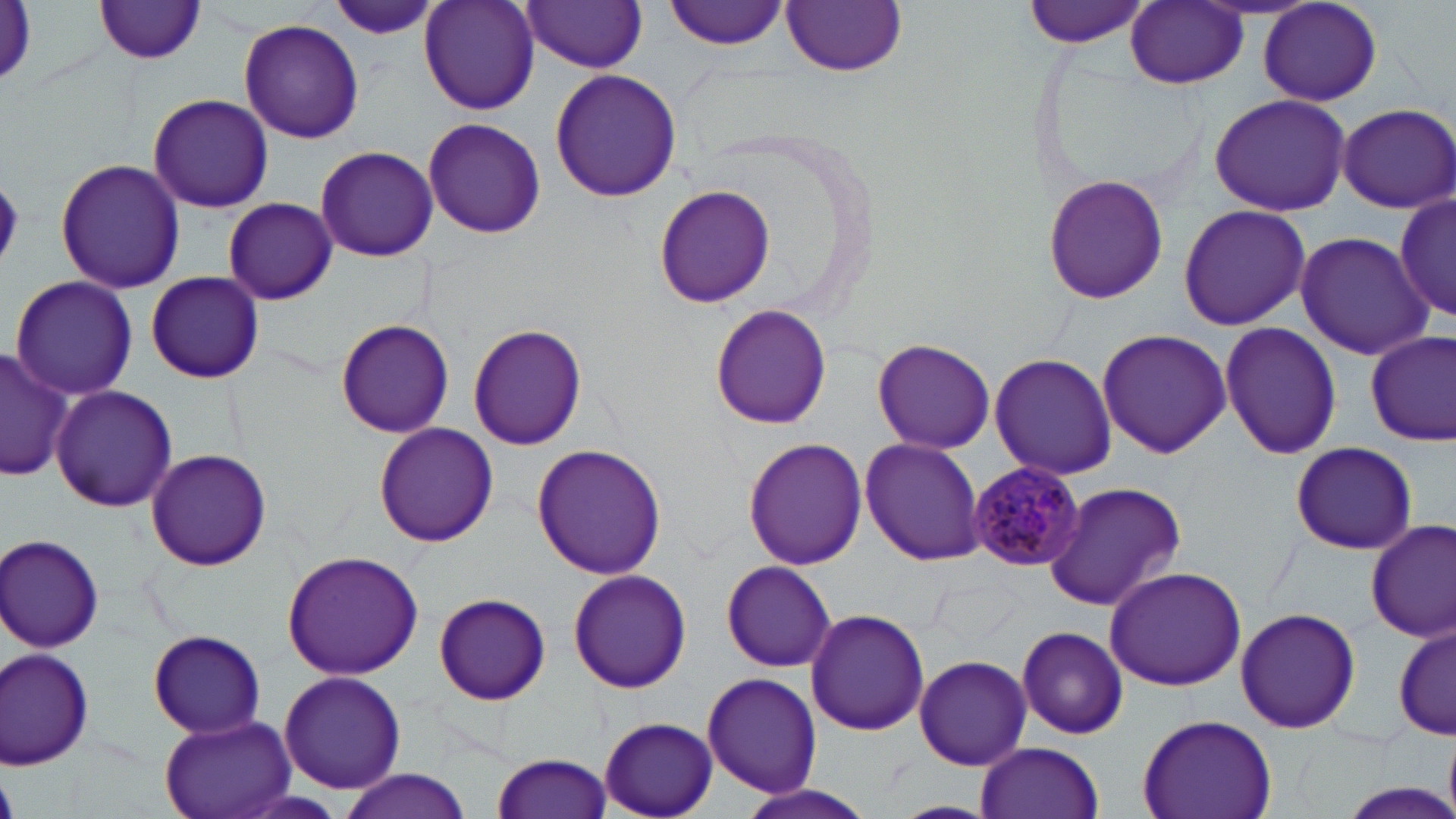

slide-level diagnosis = Plasmodium malariae
magnification = 1000x
preparation = thin blood film
modality = optical microscopy
field of view = single
stain = May-Grünwald-Giemsa
image size = 1456×819 pixels
uninfected red blood cell locations = approximate bounding boxes as named x1/y1/x2/y2 corners in pixels: (x1=419, y1=0, x2=540, y2=115), (x1=664, y1=0, x2=791, y2=50), (x1=1023, y1=0, x2=1153, y2=49), (x1=94, y1=1, x2=209, y2=64), (x1=324, y1=1, x2=442, y2=42), (x1=522, y1=1, x2=649, y2=72), (x1=782, y1=1, x2=907, y2=76), (x1=1125, y1=2, x2=1247, y2=89), (x1=1257, y1=2, x2=1383, y2=107), (x1=237, y1=20, x2=365, y2=143), (x1=550, y1=67, x2=682, y2=201), (x1=147, y1=94, x2=273, y2=212), (x1=1207, y1=94, x2=1353, y2=214), (x1=1335, y1=103, x2=1456, y2=212), (x1=422, y1=117, x2=546, y2=239), (x1=315, y1=144, x2=439, y2=261), (x1=55, y1=158, x2=186, y2=293), (x1=1044, y1=173, x2=1168, y2=304), (x1=651, y1=182, x2=775, y2=308), (x1=1392, y1=189, x2=1453, y2=325), (x1=223, y1=197, x2=337, y2=305), (x1=1177, y1=203, x2=1312, y2=331), (x1=1295, y1=231, x2=1433, y2=359), (x1=144, y1=272, x2=264, y2=383), (x1=10, y1=275, x2=139, y2=401), (x1=709, y1=304, x2=832, y2=430), (x1=335, y1=319, x2=455, y2=438), (x1=1219, y1=321, x2=1343, y2=458), (x1=468, y1=322, x2=588, y2=450), (x1=1097, y1=328, x2=1232, y2=458), (x1=1364, y1=328, x2=1455, y2=445), (x1=873, y1=338, x2=995, y2=454), (x1=0, y1=347, x2=74, y2=484), (x1=988, y1=351, x2=1119, y2=480), (x1=51, y1=385, x2=178, y2=512), (x1=375, y1=423, x2=499, y2=546), (x1=859, y1=438, x2=986, y2=566), (x1=743, y1=439, x2=868, y2=571), (x1=1286, y1=441, x2=1419, y2=554), (x1=531, y1=443, x2=667, y2=580), (x1=145, y1=447, x2=273, y2=571), (x1=1043, y1=481, x2=1187, y2=613), (x1=1366, y1=517, x2=1456, y2=644), (x1=2, y1=534, x2=105, y2=651), (x1=281, y1=550, x2=425, y2=681), (x1=718, y1=561, x2=839, y2=673), (x1=1103, y1=565, x2=1247, y2=690), (x1=567, y1=568, x2=692, y2=693), (x1=432, y1=592, x2=552, y2=706), (x1=1235, y1=606, x2=1361, y2=736), (x1=806, y1=607, x2=928, y2=736), (x1=1392, y1=617, x2=1453, y2=743), (x1=1013, y1=626, x2=1129, y2=740), (x1=148, y1=630, x2=265, y2=738), (x1=1, y1=648, x2=96, y2=771), (x1=913, y1=653, x2=1033, y2=772), (x1=278, y1=670, x2=406, y2=793), (x1=700, y1=672, x2=821, y2=797), (x1=1137, y1=712, x2=1277, y2=819), (x1=157, y1=714, x2=296, y2=819), (x1=598, y1=716, x2=718, y2=818), (x1=975, y1=741, x2=1104, y2=819), (x1=492, y1=750, x2=615, y2=818), (x1=335, y1=769, x2=475, y2=819), (x1=738, y1=779, x2=883, y2=819)
Plasmodium malariae-infected red blood cell locations = approximate bounding boxes as named x1/y1/x2/y2 corners in pixels: (x1=971, y1=462, x2=1086, y2=571)